Report the malaria status of this cell.
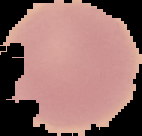
It is uninfected.

Image is 142×136 pixels. Cell region segmented out of the field of view; the surrounding area is masked to black. From a thin blood film.